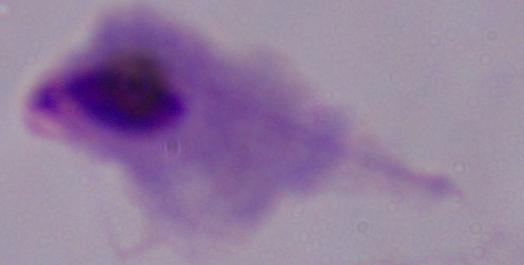

Summary:
  - Modality: photomicrograph
  - Magnification: 1000x
  - Identification: trichomonad